Report the malaria status of this cell.
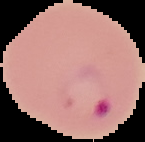
Parasitized.

preparation: thin blood smear
image_size: 145×142 pixels
image_type: segmented cell region on a black background